Assess this cell for malaria.
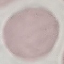
Uninfected.

{
  "image_type": "automatically extracted cell patch, resized to 64 × 64 pixels",
  "stain": "Giemsa",
  "capture": "smartphone camera at the microscope eyepiece",
  "preparation": "thin smear"
}